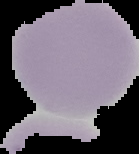

Cell region segmented out of the field of view; the surrounding area is masked to black. Result: no malaria parasites seen. From a thin blood film. Image is 139×154 pixels.